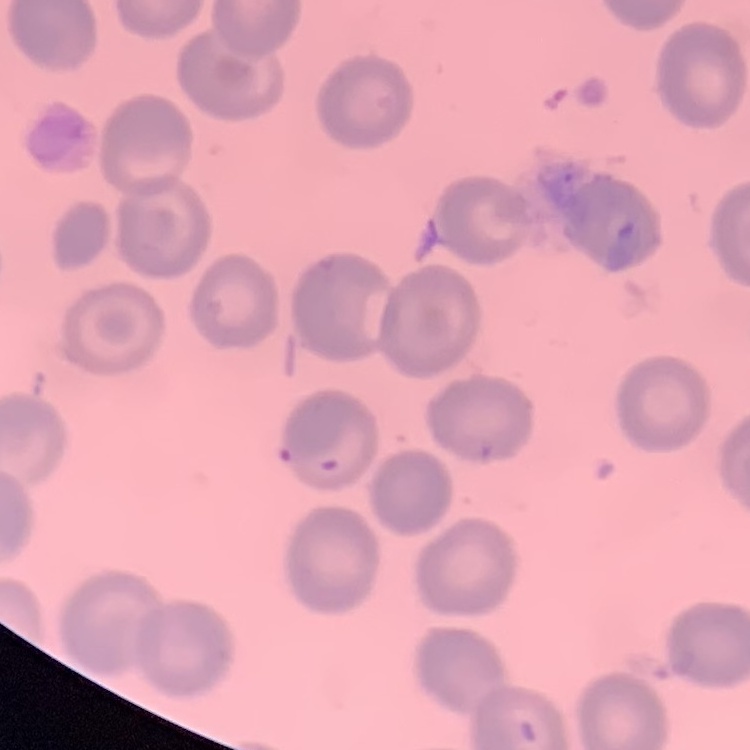
erythrocyte morphology = no rouleaux formation
preparation = thin blood smear
stain = Field's or Giemsa
image type = square crop of a larger photomicrograph